Locate every malaria parasite.
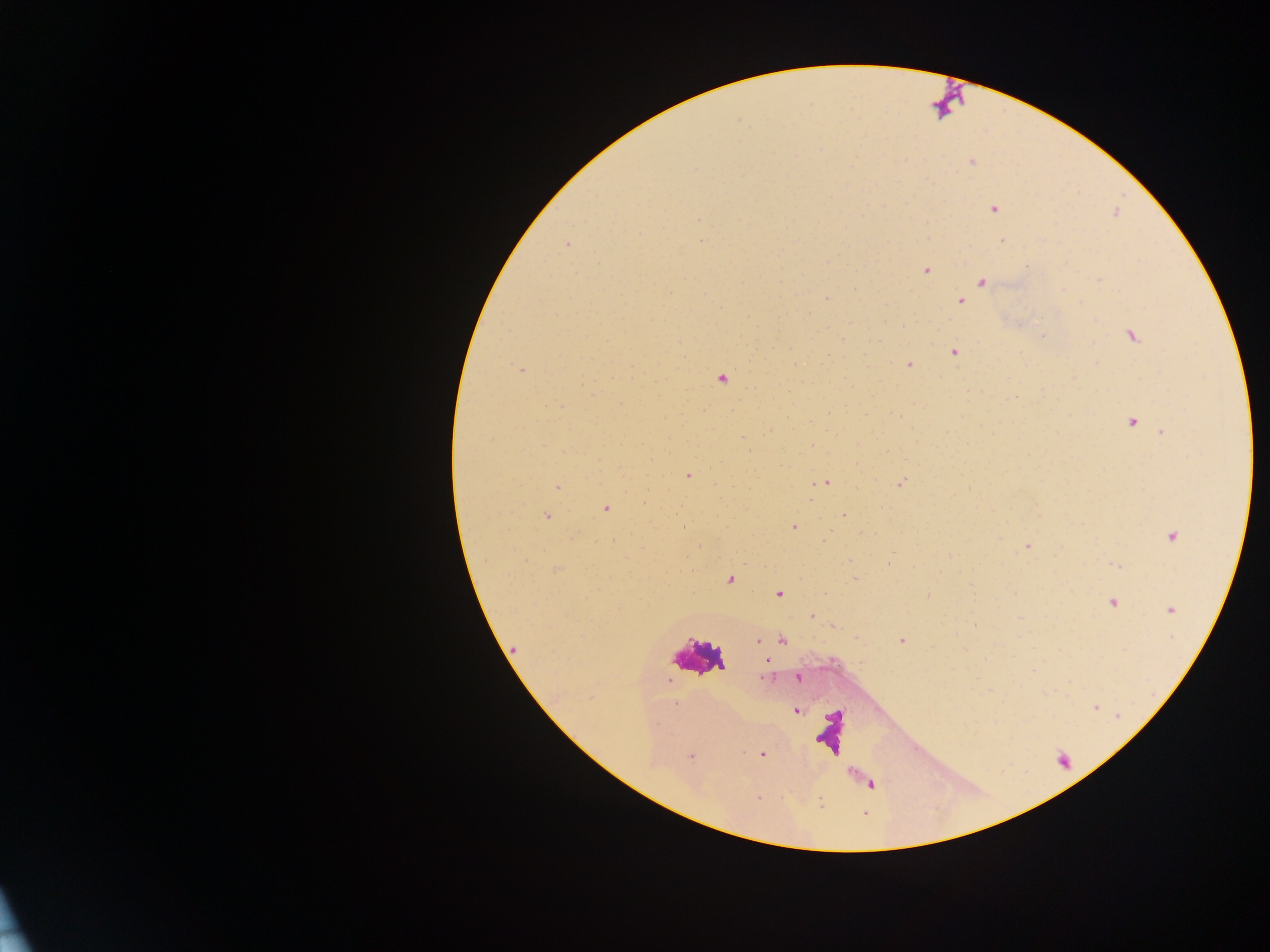

Approximate centers as {x, y} in pixels.
Malaria parasites: {971, 163}, {993, 210}, {700, 219}, {1002, 240}, {702, 241}, {567, 244}, {925, 272}, {1099, 280}, {981, 281}, {827, 297}, {960, 300}, {720, 307}, {884, 320}, {902, 325}, {1131, 334}, {841, 339}, {954, 353}, {909, 364}, {521, 369}, {628, 375}, {723, 378}, {584, 385}, {1008, 398}, {898, 417}, {1132, 420}, {741, 438}, {687, 475}, {829, 482}, {900, 483}, {560, 487}, {967, 488}, {607, 509}, {845, 513}, {548, 516}, {794, 527}, {829, 532}, {1170, 535}, {1026, 546}, {893, 552}, {948, 555}, {847, 559}, {1116, 565}, {854, 578}, {729, 579}, {780, 594}, {1114, 603}, {1169, 610}, {813, 616}, {1020, 617}, {975, 625}, {834, 627}, {756, 640}, {900, 641}, {765, 662}, {764, 676}, {798, 678}, {675, 703}, {797, 710}, {655, 722}, {762, 754}, {690, 755}, {756, 799}, {818, 804}.

One field of view. Collected in Ghana. Image is 1270×952 pixels. Mobile-phone photograph taken through the microscope. Thick blood smear.